State which parasite is depicted.
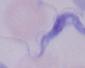
A trypanosome.

Photomicrograph. Captured at 1000x magnification.